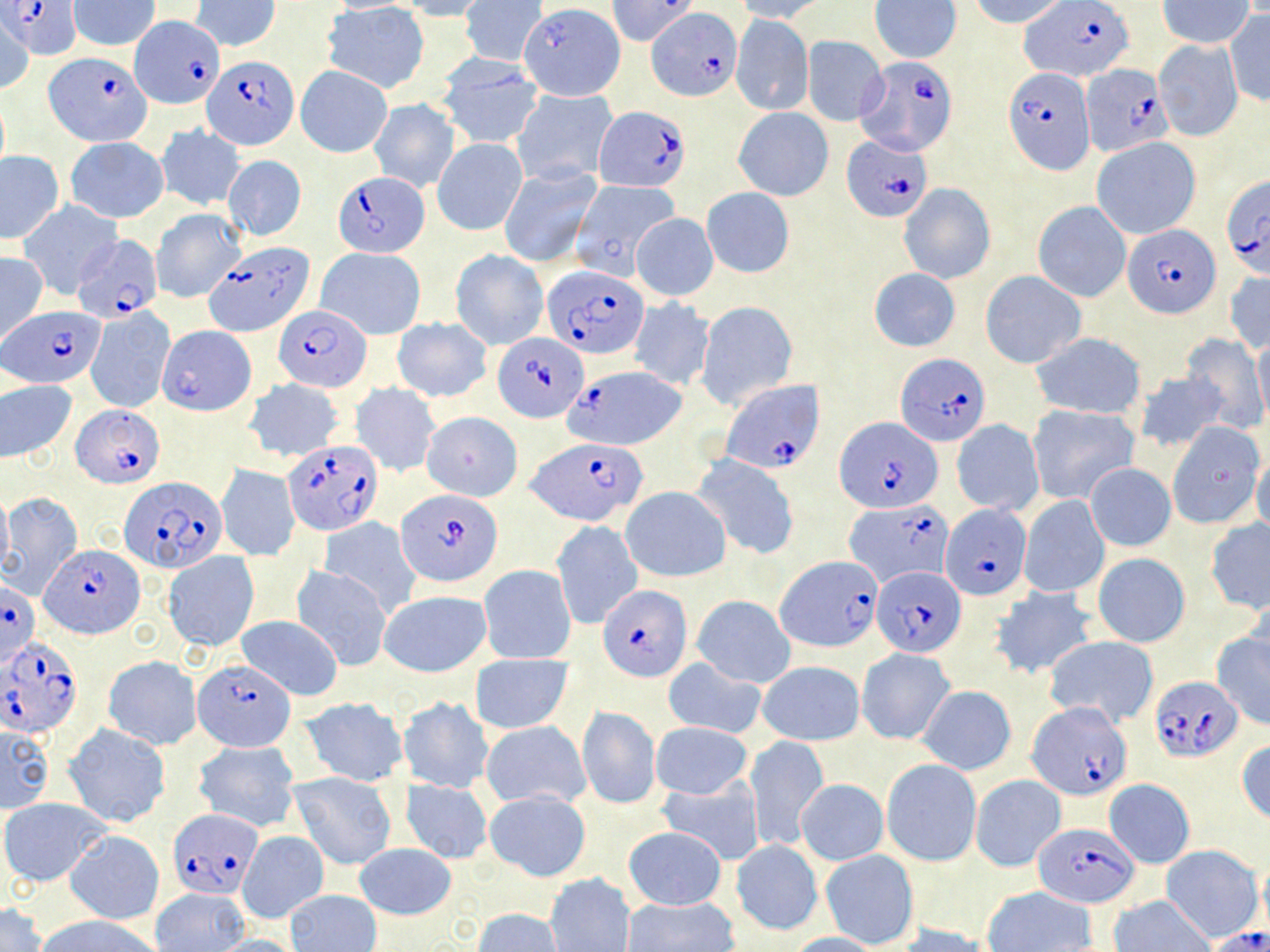

plasmodium_falciparum_infected_red_blood_cell_locations_subset: 'approximate bounding boxes as named x1/y1/x2/y2 corners in pixels: (x1=7, y1=0, x2=80, y2=60), (x1=608, y1=0, x2=701, y2=46), (x1=1019, y1=2, x2=1137, y2=80), (x1=648, y1=9, x2=739, y2=97), (x1=129, y1=15, x2=225, y2=109), (x1=202, y1=53, x2=298, y2=150), (x1=855, y1=53, x2=957, y2=175), (x1=1080, y1=66, x2=1174, y2=157), (x1=1004, y1=69, x2=1095, y2=173), (x1=594, y1=105, x2=690, y2=192), (x1=844, y1=140, x2=932, y2=220), (x1=332, y1=171, x2=430, y2=258), (x1=1221, y1=175, x2=1270, y2=278), (x1=1124, y1=227, x2=1221, y2=319), (x1=71, y1=234, x2=164, y2=326), (x1=206, y1=240, x2=313, y2=336), (x1=543, y1=264, x2=649, y2=359), (x1=5, y1=305, x2=103, y2=387), (x1=274, y1=305, x2=372, y2=393), (x1=496, y1=335, x2=588, y2=422), (x1=896, y1=353, x2=991, y2=445), (x1=565, y1=364, x2=685, y2=451), (x1=719, y1=380, x2=823, y2=473), (x1=73, y1=405, x2=161, y2=485), (x1=836, y1=417, x2=943, y2=513), (x1=282, y1=438, x2=381, y2=532), (x1=527, y1=438, x2=648, y2=525), (x1=120, y1=476, x2=226, y2=573), (x1=398, y1=488, x2=503, y2=586), (x1=843, y1=502, x2=954, y2=588), (x1=940, y1=504, x2=1030, y2=600), (x1=40, y1=545, x2=143, y2=638), (x1=777, y1=556, x2=886, y2=652), (x1=872, y1=564, x2=966, y2=658), (x1=1, y1=581, x2=41, y2=669), (x1=599, y1=584, x2=690, y2=681), (x1=0, y1=635, x2=84, y2=738), (x1=194, y1=656, x2=295, y2=751), (x1=1149, y1=676, x2=1242, y2=763), (x1=1028, y1=704, x2=1133, y2=800), (x1=170, y1=808, x2=263, y2=899), (x1=1033, y1=822, x2=1139, y2=907)'
slide_level_diagnosis: Plasmodium falciparum
field_of_view: one of a larger specimen
modality: optical microscopy
magnification: 1000x
image_size: 1270×952 pixels
stain: May-Grünwald-Giemsa
preparation: thin blood smear
uninfected_red_blood_cell_locations_subset: 'approximate bounding boxes as named x1/y1/x2/y2 corners in pixels: (x1=69, y1=0, x2=160, y2=51), (x1=461, y1=0, x2=546, y2=66), (x1=732, y1=0, x2=832, y2=23), (x1=967, y1=0, x2=1072, y2=27), (x1=1156, y1=0, x2=1256, y2=48), (x1=192, y1=1, x2=280, y2=52), (x1=401, y1=1, x2=493, y2=21), (x1=868, y1=1, x2=961, y2=63), (x1=520, y1=3, x2=623, y2=100), (x1=322, y1=4, x2=431, y2=94), (x1=1225, y1=8, x2=1270, y2=106), (x1=731, y1=12, x2=813, y2=116), (x1=1, y1=13, x2=36, y2=93), (x1=801, y1=35, x2=887, y2=126), (x1=1152, y1=39, x2=1243, y2=141), (x1=434, y1=58, x2=545, y2=150), (x1=297, y1=66, x2=392, y2=157), (x1=511, y1=87, x2=616, y2=186), (x1=368, y1=99, x2=461, y2=192), (x1=734, y1=107, x2=833, y2=200), (x1=157, y1=126, x2=245, y2=209), (x1=65, y1=136, x2=170, y2=223), (x1=433, y1=137, x2=527, y2=236), (x1=1091, y1=137, x2=1200, y2=238), (x1=1, y1=150, x2=66, y2=243), (x1=223, y1=153, x2=308, y2=242), (x1=500, y1=165, x2=601, y2=268), (x1=571, y1=177, x2=681, y2=275), (x1=898, y1=183, x2=996, y2=284), (x1=701, y1=187, x2=795, y2=278), (x1=18, y1=200, x2=122, y2=298), (x1=1033, y1=200, x2=1132, y2=302), (x1=152, y1=208, x2=244, y2=302), (x1=631, y1=213, x2=718, y2=301), (x1=316, y1=246, x2=426, y2=340), (x1=450, y1=249, x2=548, y2=350), (x1=0, y1=252, x2=48, y2=346), (x1=867, y1=267, x2=962, y2=352), (x1=1225, y1=269, x2=1269, y2=355), (x1=981, y1=271, x2=1086, y2=368), (x1=628, y1=298, x2=715, y2=391), (x1=697, y1=301, x2=799, y2=408), (x1=85, y1=308, x2=174, y2=413), (x1=391, y1=316, x2=492, y2=402), (x1=158, y1=326, x2=256, y2=416), (x1=1028, y1=332, x2=1147, y2=421), (x1=1181, y1=334, x2=1268, y2=434), (x1=1252, y1=335, x2=1270, y2=430), (x1=1131, y1=369, x2=1230, y2=454), (x1=0, y1=378, x2=76, y2=463), (x1=242, y1=378, x2=347, y2=462), (x1=351, y1=383, x2=440, y2=476), (x1=1026, y1=404, x2=1140, y2=503), (x1=421, y1=410, x2=522, y2=501), (x1=951, y1=420, x2=1044, y2=515), (x1=1168, y1=422, x2=1265, y2=528), (x1=693, y1=454, x2=800, y2=559), (x1=1252, y1=455, x2=1270, y2=537), (x1=1085, y1=463, x2=1176, y2=551), (x1=217, y1=464, x2=300, y2=560), (x1=621, y1=486, x2=730, y2=582), (x1=0, y1=487, x2=12, y2=575), (x1=1, y1=492, x2=84, y2=598), (x1=1019, y1=496, x2=1110, y2=598), (x1=320, y1=517, x2=421, y2=617), (x1=551, y1=520, x2=642, y2=629), (x1=1204, y1=520, x2=1270, y2=613), (x1=164, y1=551, x2=257, y2=651), (x1=1092, y1=555, x2=1190, y2=646), (x1=478, y1=563, x2=577, y2=664), (x1=291, y1=564, x2=393, y2=670), (x1=990, y1=584, x2=1099, y2=681), (x1=379, y1=590, x2=491, y2=677), (x1=693, y1=595, x2=795, y2=688), (x1=235, y1=614, x2=343, y2=700), (x1=1212, y1=630, x2=1270, y2=730), (x1=1044, y1=636, x2=1160, y2=727), (x1=857, y1=648, x2=956, y2=744), (x1=470, y1=654, x2=574, y2=735), (x1=103, y1=656, x2=201, y2=749), (x1=662, y1=658, x2=766, y2=738), (x1=757, y1=660, x2=865, y2=745), (x1=918, y1=685, x2=1016, y2=774), (x1=399, y1=695, x2=492, y2=793), (x1=303, y1=697, x2=405, y2=787), (x1=577, y1=706, x2=660, y2=808), (x1=481, y1=721, x2=591, y2=809), (x1=651, y1=722, x2=752, y2=800), (x1=1, y1=723, x2=54, y2=813), (x1=65, y1=725, x2=169, y2=827), (x1=743, y1=735, x2=829, y2=851), (x1=1236, y1=738, x2=1270, y2=825), (x1=193, y1=739, x2=300, y2=833), (x1=882, y1=759, x2=981, y2=866), (x1=288, y1=771, x2=398, y2=871), (x1=971, y1=775, x2=1066, y2=871), (x1=656, y1=778, x2=765, y2=864), (x1=796, y1=778, x2=889, y2=865), (x1=403, y1=779, x2=492, y2=864), (x1=1105, y1=780, x2=1195, y2=869), (x1=484, y1=789, x2=592, y2=881), (x1=0, y1=798, x2=109, y2=887), (x1=622, y1=827, x2=727, y2=911), (x1=64, y1=830, x2=163, y2=925), (x1=237, y1=831, x2=328, y2=923), (x1=731, y1=840, x2=822, y2=935), (x1=355, y1=841, x2=456, y2=918), (x1=1162, y1=845, x2=1261, y2=941), (x1=820, y1=849, x2=920, y2=949), (x1=1256, y1=856, x2=1270, y2=944), (x1=546, y1=873, x2=635, y2=952), (x1=152, y1=887, x2=249, y2=952), (x1=983, y1=887, x2=1097, y2=952), (x1=286, y1=889, x2=381, y2=952), (x1=1110, y1=895, x2=1216, y2=952), (x1=621, y1=897, x2=738, y2=952), (x1=0, y1=904, x2=46, y2=952), (x1=472, y1=908, x2=564, y2=952), (x1=40, y1=916, x2=162, y2=952), (x1=896, y1=924, x2=1000, y2=951), (x1=1205, y1=927, x2=1270, y2=952), (x1=783, y1=931, x2=886, y2=952), (x1=212, y1=934, x2=307, y2=952)'